State which parasite is depicted.
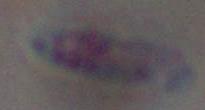
Toxoplasma gondii.

Summary:
  - Modality: micrograph
  - Magnification: 1000x